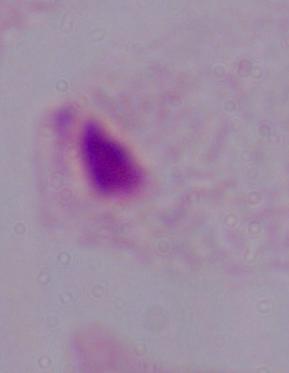

Micrograph. Captured at 1000x magnification. A trichomonad is seen.